Classify this cell by malaria status.
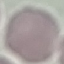

Uninfected.

Automatically extracted cell patch, resized to 64 × 64 pixels. Acquired by smartphone through the microscope eyepiece. Thin blood film. Giemsa-stained preparation.